Locate every Plasmodium parasite.
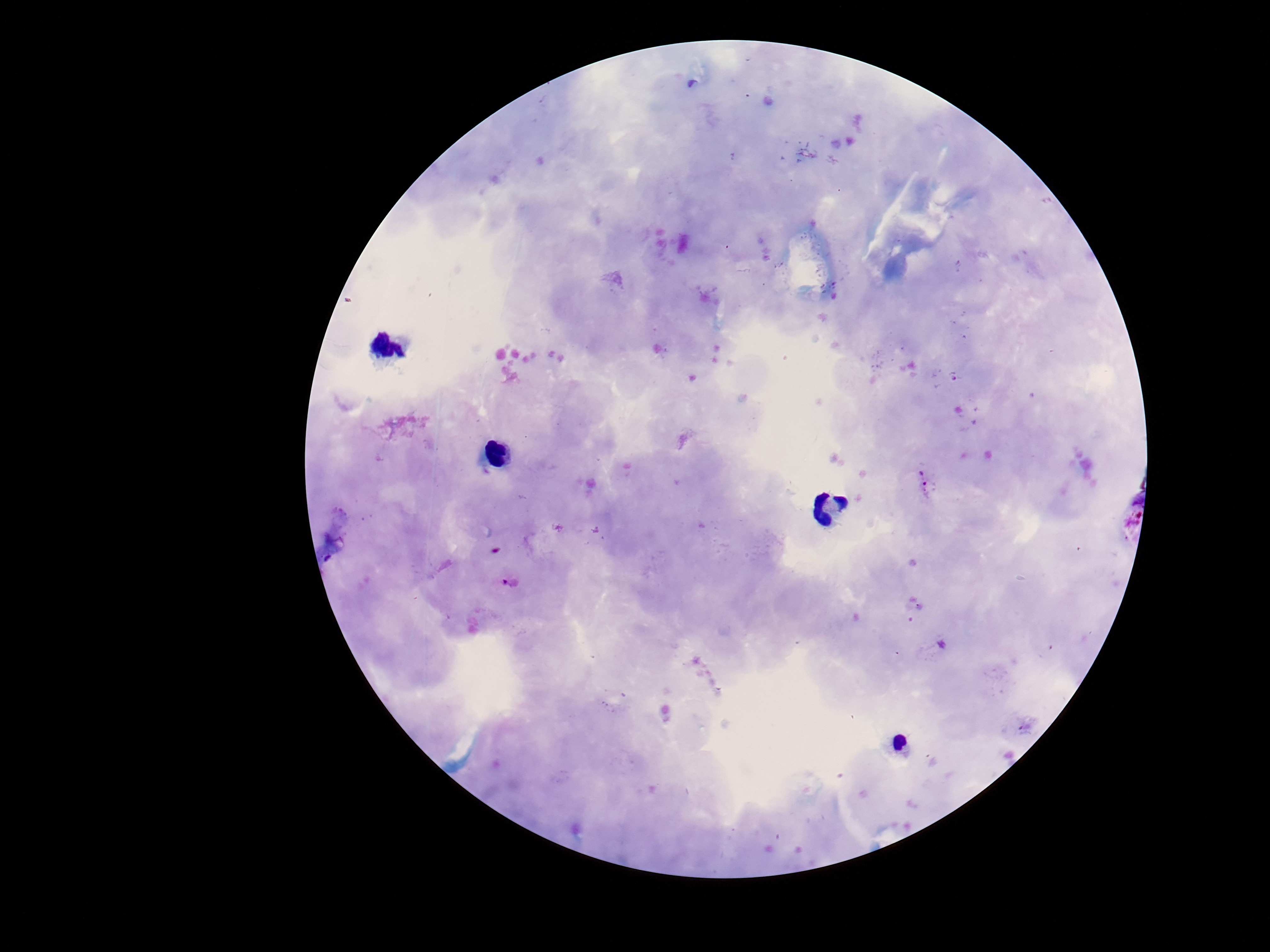

Approximate centers as {x, y} in pixels.
Plasmodium parasites: {925, 480}, {507, 582}.

Photographed through the microscope eyepiece with a smartphone camera. Thick blood smear. 100x magnification. Image is 1270×952 pixels. Patient malaria status: positive. One field from this slide. Giemsa-stained preparation.